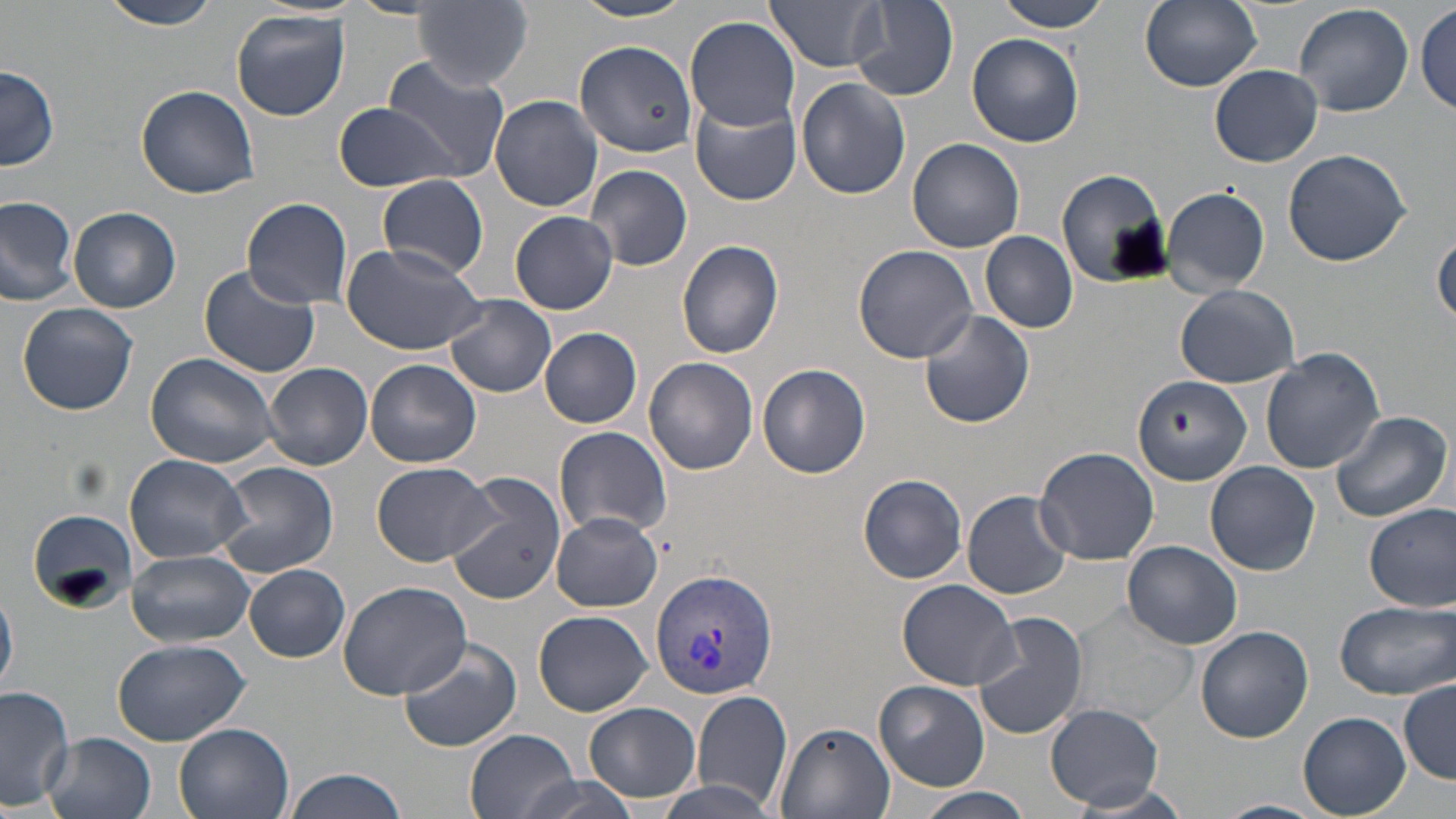
Plasmodium vivax-infected red blood cell locations = approximate bounding boxes as [x1, y1, x2, y2] in pixels: [650, 571, 777, 698]
slide-level diagnosis = Plasmodium vivax
preparation = thin blood film
modality = optical microscopy
field of view = one of a larger specimen
image size = 1456×819 pixels
magnification = 1000x
uninfected red blood cell locations = approximate bounding boxes as [x1, y1, x2, y2] in pixels: [100, 0, 223, 32], [410, 0, 534, 91], [572, 0, 692, 23], [765, 0, 888, 72], [993, 0, 1114, 32], [1138, 0, 1263, 94], [850, 1, 958, 101], [1294, 3, 1413, 116], [1413, 3, 1454, 116], [232, 11, 350, 121], [685, 17, 802, 131], [967, 33, 1085, 148], [575, 39, 698, 159], [381, 58, 510, 180], [1209, 64, 1323, 167], [1, 65, 60, 172], [796, 79, 911, 200], [135, 84, 257, 200], [488, 96, 604, 212], [691, 100, 801, 206], [333, 102, 457, 192], [908, 137, 1025, 252], [1283, 147, 1411, 266], [585, 164, 692, 271], [1048, 166, 1175, 287], [376, 174, 489, 279], [1163, 185, 1270, 294], [0, 193, 78, 308], [244, 196, 354, 309], [69, 206, 181, 312], [511, 211, 618, 314], [980, 231, 1078, 333], [1431, 232, 1456, 327], [675, 240, 784, 360], [339, 242, 486, 355], [853, 245, 980, 363], [201, 264, 323, 381], [1175, 283, 1300, 387], [445, 296, 557, 397], [16, 303, 139, 417], [917, 309, 1035, 429], [540, 327, 641, 427], [1260, 348, 1385, 473], [145, 352, 281, 469], [366, 358, 481, 468], [644, 358, 758, 474], [263, 363, 373, 469], [756, 363, 872, 479], [1131, 374, 1250, 486], [1331, 411, 1452, 526], [552, 425, 672, 540], [1035, 447, 1161, 566], [126, 453, 250, 564], [214, 460, 338, 577], [372, 462, 497, 565], [1205, 462, 1320, 576], [442, 474, 567, 603], [858, 474, 969, 584], [963, 492, 1074, 600], [1364, 502, 1456, 612], [24, 507, 138, 611], [551, 512, 662, 612], [1123, 540, 1241, 649], [126, 551, 254, 647], [244, 564, 351, 663], [336, 579, 472, 700], [897, 579, 1022, 690], [0, 586, 19, 696], [1336, 600, 1456, 698], [532, 610, 653, 717], [971, 612, 1089, 741], [1079, 623, 1196, 724], [1195, 626, 1313, 742], [397, 636, 527, 753], [112, 638, 252, 746], [1398, 679, 1455, 782], [875, 681, 990, 790], [0, 684, 76, 811], [692, 689, 793, 811], [583, 701, 702, 802], [1045, 703, 1165, 810], [1298, 711, 1411, 818], [174, 722, 295, 819], [776, 722, 895, 819], [466, 729, 579, 819], [44, 731, 157, 819], [286, 768, 405, 819], [513, 775, 645, 819], [644, 779, 786, 819], [1068, 783, 1195, 819], [913, 789, 1035, 819], [1212, 799, 1326, 819]
stain = May-Grünwald-Giemsa